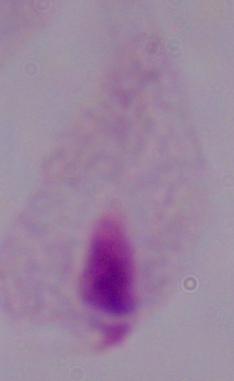
1000x magnification. A trichomonad is seen. Photomicrograph.